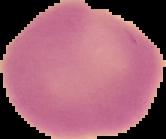

Summary:
  - Preparation: thin blood smear
  - Image type: segmented cell region with the area outside set to black
  - Result: negative for Plasmodium parasites
  - Image size: 166×139 pixels